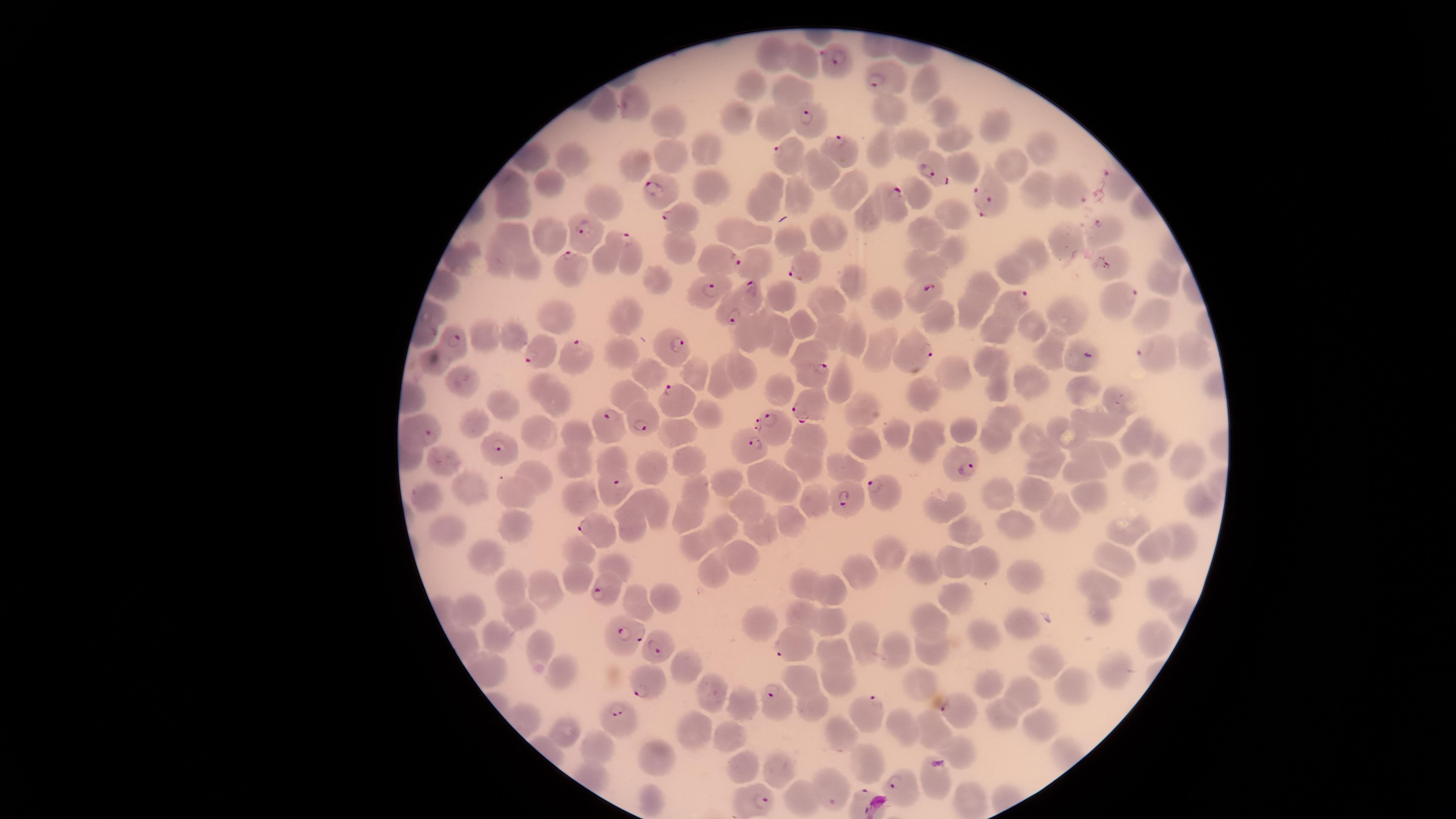

Approximate marker points, in pixels from the top-left corner.
Summary:
  - Uninfected red blood cells: (x=772, y=52), (x=798, y=64), (x=925, y=81), (x=794, y=89), (x=755, y=90), (x=886, y=108), (x=945, y=115), (x=665, y=120), (x=739, y=122), (x=777, y=122), (x=998, y=123), (x=951, y=135), (x=915, y=140), (x=881, y=144), (x=704, y=145), (x=1042, y=148), (x=531, y=156), (x=673, y=158), (x=571, y=161), (x=636, y=164), (x=1013, y=166), (x=816, y=167), (x=969, y=170), (x=512, y=180), (x=545, y=182), (x=843, y=186), (x=1038, y=187), (x=709, y=189), (x=915, y=189), (x=767, y=193), (x=796, y=193), (x=602, y=198), (x=514, y=205), (x=952, y=214), (x=873, y=219), (x=550, y=235), (x=745, y=235), (x=794, y=235), (x=823, y=235), (x=928, y=235), (x=517, y=236), (x=1072, y=239), (x=606, y=250), (x=681, y=250), (x=1039, y=250), (x=954, y=252), (x=499, y=261), (x=754, y=261), (x=926, y=263), (x=1017, y=268), (x=529, y=270), (x=657, y=278), (x=1158, y=278), (x=854, y=281), (x=986, y=287), (x=780, y=299), (x=827, y=301), (x=892, y=303), (x=1067, y=312), (x=625, y=313), (x=972, y=313), (x=939, y=314), (x=1150, y=319), (x=561, y=320), (x=799, y=323), (x=1033, y=325), (x=768, y=328), (x=1000, y=329), (x=749, y=333), (x=828, y=333), (x=513, y=335), (x=484, y=336), (x=782, y=337), (x=855, y=339), (x=882, y=348), (x=620, y=350), (x=1052, y=350), (x=1190, y=351), (x=987, y=358), (x=434, y=362), (x=806, y=362), (x=651, y=372), (x=745, y=373), (x=956, y=375), (x=696, y=376), (x=720, y=379), (x=461, y=380), (x=1033, y=384), (x=780, y=386), (x=841, y=387), (x=1001, y=387), (x=924, y=389), (x=1088, y=390), (x=553, y=400), (x=629, y=400), (x=1120, y=402), (x=505, y=408), (x=862, y=409), (x=705, y=415), (x=1008, y=415), (x=1108, y=420), (x=480, y=422), (x=966, y=428), (x=895, y=431), (x=1061, y=431), (x=547, y=433), (x=681, y=433), (x=1139, y=434), (x=576, y=435), (x=932, y=436), (x=807, y=437), (x=993, y=439), (x=1035, y=440), (x=862, y=444), (x=1159, y=448), (x=921, y=453), (x=1114, y=454), (x=687, y=456), (x=799, y=456), (x=1083, y=456), (x=1188, y=458), (x=575, y=462), (x=610, y=463), (x=1050, y=463), (x=447, y=464), (x=842, y=465), (x=655, y=466), (x=758, y=471), (x=1083, y=471), (x=538, y=472), (x=1139, y=478), (x=725, y=480), (x=695, y=484), (x=473, y=485), (x=791, y=487), (x=517, y=492), (x=1032, y=493), (x=997, y=494), (x=579, y=495), (x=426, y=496), (x=1089, y=499), (x=650, y=501), (x=814, y=501), (x=1197, y=502), (x=747, y=505), (x=943, y=510), (x=1065, y=511), (x=685, y=518), (x=787, y=520), (x=629, y=522), (x=518, y=523), (x=722, y=525), (x=1017, y=528), (x=1129, y=529), (x=448, y=530), (x=759, y=531), (x=966, y=534), (x=1184, y=542), (x=699, y=546), (x=1160, y=547), (x=488, y=550), (x=576, y=552), (x=891, y=554), (x=1118, y=555), (x=744, y=557), (x=614, y=565), (x=959, y=566), (x=982, y=566), (x=717, y=567), (x=925, y=567), (x=860, y=570), (x=573, y=576), (x=1026, y=577), (x=1102, y=583), (x=803, y=584), (x=506, y=588), (x=540, y=589), (x=836, y=591), (x=1167, y=591), (x=668, y=598), (x=960, y=602), (x=638, y=605), (x=468, y=611), (x=1098, y=611), (x=522, y=616), (x=803, y=616), (x=764, y=621), (x=833, y=622), (x=939, y=622), (x=1024, y=626), (x=496, y=638), (x=1152, y=638), (x=990, y=639), (x=863, y=642), (x=541, y=648), (x=834, y=650), (x=895, y=651), (x=936, y=654), (x=1044, y=659), (x=690, y=666), (x=1114, y=670), (x=559, y=671), (x=806, y=679), (x=988, y=681), (x=843, y=682), (x=925, y=686), (x=1074, y=686), (x=1025, y=691), (x=710, y=693), (x=815, y=704), (x=747, y=705), (x=1004, y=718), (x=1037, y=720), (x=561, y=727), (x=906, y=727), (x=937, y=728), (x=692, y=732), (x=727, y=732), (x=840, y=735), (x=601, y=745), (x=961, y=751), (x=658, y=757), (x=867, y=765), (x=744, y=766), (x=779, y=769), (x=939, y=780), (x=799, y=797), (x=971, y=799), (x=645, y=804)
  - Parasitized red blood cells: (x=834, y=62), (x=884, y=74), (x=806, y=122), (x=837, y=146), (x=791, y=152), (x=933, y=170), (x=1113, y=178), (x=658, y=191), (x=990, y=192), (x=1073, y=193), (x=893, y=200), (x=676, y=217), (x=1104, y=230), (x=587, y=241), (x=633, y=257), (x=721, y=260), (x=571, y=269), (x=803, y=270), (x=925, y=291), (x=1119, y=291), (x=753, y=294), (x=703, y=296), (x=1019, y=303), (x=731, y=316), (x=676, y=349), (x=462, y=350), (x=1150, y=351), (x=1075, y=352), (x=541, y=355), (x=578, y=356), (x=922, y=358), (x=814, y=373), (x=673, y=397), (x=811, y=409), (x=642, y=418), (x=771, y=421), (x=604, y=425), (x=428, y=432), (x=749, y=441), (x=502, y=450), (x=961, y=464), (x=616, y=486), (x=876, y=489), (x=846, y=502), (x=595, y=530), (x=600, y=590), (x=622, y=634), (x=792, y=643), (x=660, y=653), (x=648, y=688), (x=776, y=696), (x=869, y=709), (x=954, y=713), (x=622, y=717), (x=903, y=785), (x=834, y=796), (x=761, y=804)
  - Capture: smartphone photograph through the microscope eyepiece
  - Preparation: thin blood film
  - Field of view: single
  - Species: Plasmodium falciparum
  - Image size: 1456×819 pixels
  - Visible region: circular
  - Presence: malaria parasites seen
  - Stain: Giemsa